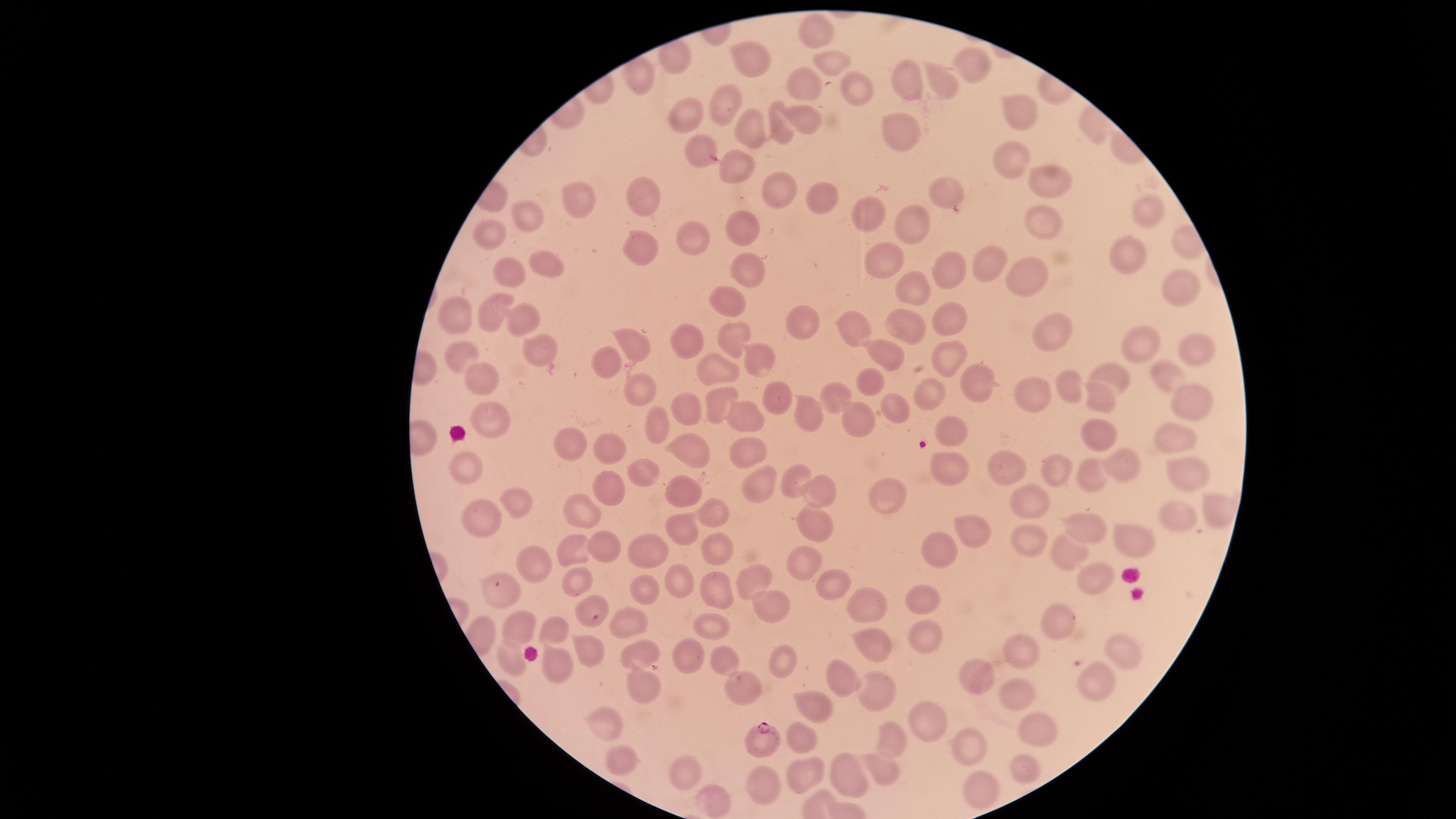
Approximate marker points as {x, y} in pixels. Uninfected red blood cells: {814, 27}, {756, 58}, {823, 61}, {971, 68}, {912, 76}, {634, 77}, {856, 82}, {945, 84}, {804, 91}, {730, 98}, {1018, 107}, {805, 110}, {691, 113}, {782, 125}, {748, 129}, {894, 131}, {697, 148}, {1007, 161}, {741, 167}, {777, 179}, {1051, 179}, {944, 193}, {580, 196}, {650, 196}, {819, 197}, {872, 208}, {1142, 210}, {524, 212}, {1035, 223}, {922, 225}, {696, 230}, {740, 230}, {494, 231}, {640, 246}, {887, 256}, {1127, 256}, {547, 261}, {981, 264}, {509, 273}, {950, 273}, {747, 274}, {1036, 276}, {1174, 288}, {911, 290}, {729, 301}, {455, 312}, {493, 313}, {521, 317}, {799, 317}, {941, 319}, {905, 326}, {863, 330}, {738, 331}, {1049, 333}, {687, 342}, {636, 343}, {1139, 343}, {538, 349}, {950, 352}, {753, 353}, {1198, 353}, {464, 356}, {884, 357}, {611, 358}, {1170, 373}, {719, 375}, {1122, 376}, {476, 378}, {979, 380}, {642, 385}, {1067, 385}, {876, 386}, {933, 393}, {834, 394}, {1021, 394}, {779, 396}, {716, 397}, {1100, 397}, {678, 407}, {1194, 408}, {896, 410}, {801, 413}, {747, 417}, {494, 419}, {655, 422}, {864, 425}, {955, 431}, {1101, 433}, {1163, 433}, {577, 443}, {694, 448}, {748, 448}, {614, 450}, {465, 461}, {950, 461}, {1121, 462}, {1054, 467}, {642, 468}, {1185, 470}, {1008, 471}, {796, 474}, {1090, 476}, {758, 480}, {818, 488}, {609, 489}, {681, 493}, {883, 493}, {527, 502}, {1028, 503}, {1205, 506}, {585, 509}, {477, 512}, {713, 512}, {1176, 518}, {1083, 525}, {814, 526}, {970, 526}, {680, 527}, {1129, 537}, {1031, 538}, {713, 542}, {600, 544}, {938, 547}, {572, 549}, {640, 550}, {1062, 551}, {801, 561}, {534, 562}, {1093, 570}, {749, 577}, {585, 580}, {681, 580}, {820, 581}, {647, 584}, {717, 589}, {503, 593}, {925, 601}, {586, 606}, {865, 608}, {770, 609}, {1062, 621}, {624, 622}, {711, 626}, {514, 627}, {555, 631}, {926, 634}, {865, 641}, {1021, 646}, {1122, 648}, {638, 649}, {593, 653}, {690, 654}, {782, 658}, {515, 659}, {718, 659}, {554, 663}, {849, 676}, {974, 677}, {1093, 681}, {640, 685}, {739, 685}, {873, 687}, {1016, 693}, {815, 700}, {920, 723}, {609, 726}, {1035, 726}, {799, 735}, {895, 740}, {968, 743}, {621, 759}, {691, 765}, {885, 767}, {1023, 769}, {854, 770}, {807, 775}, {769, 783}, {983, 787}, {711, 806}. Parasitized red blood cells: {761, 737}. Presence: malaria parasites seen. Smartphone photograph through the microscope eyepiece. One field of view of the specimen. Thin blood film. Image is 1456×819 pixels. The visible region is circular. Species: Plasmodium falciparum. Giemsa stain.